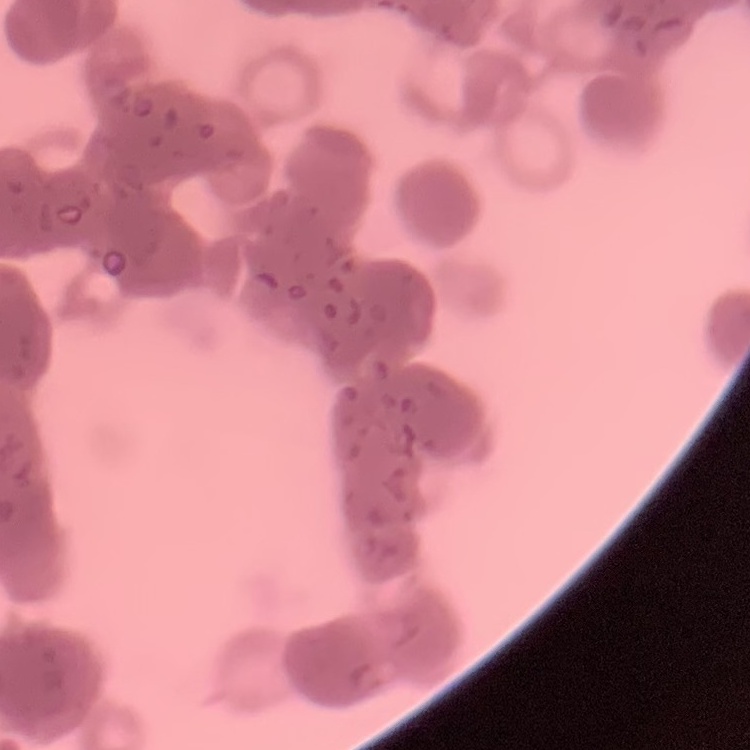

Summary:
  - Red blood cell morphology: rouleaux formation
  - Stain: Field's or Giemsa
  - Preparation: thin blood smear
  - Image type: square crop of a larger photomicrograph